Assess this cell for malaria.
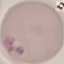
It is parasitized.

Summary:
  - Capture: smartphone camera at the microscope eyepiece
  - Preparation: thin smear
  - Image type: automatically extracted cell patch, resized to 64 × 64 pixels
  - Stain: Giemsa